Outline platelets.
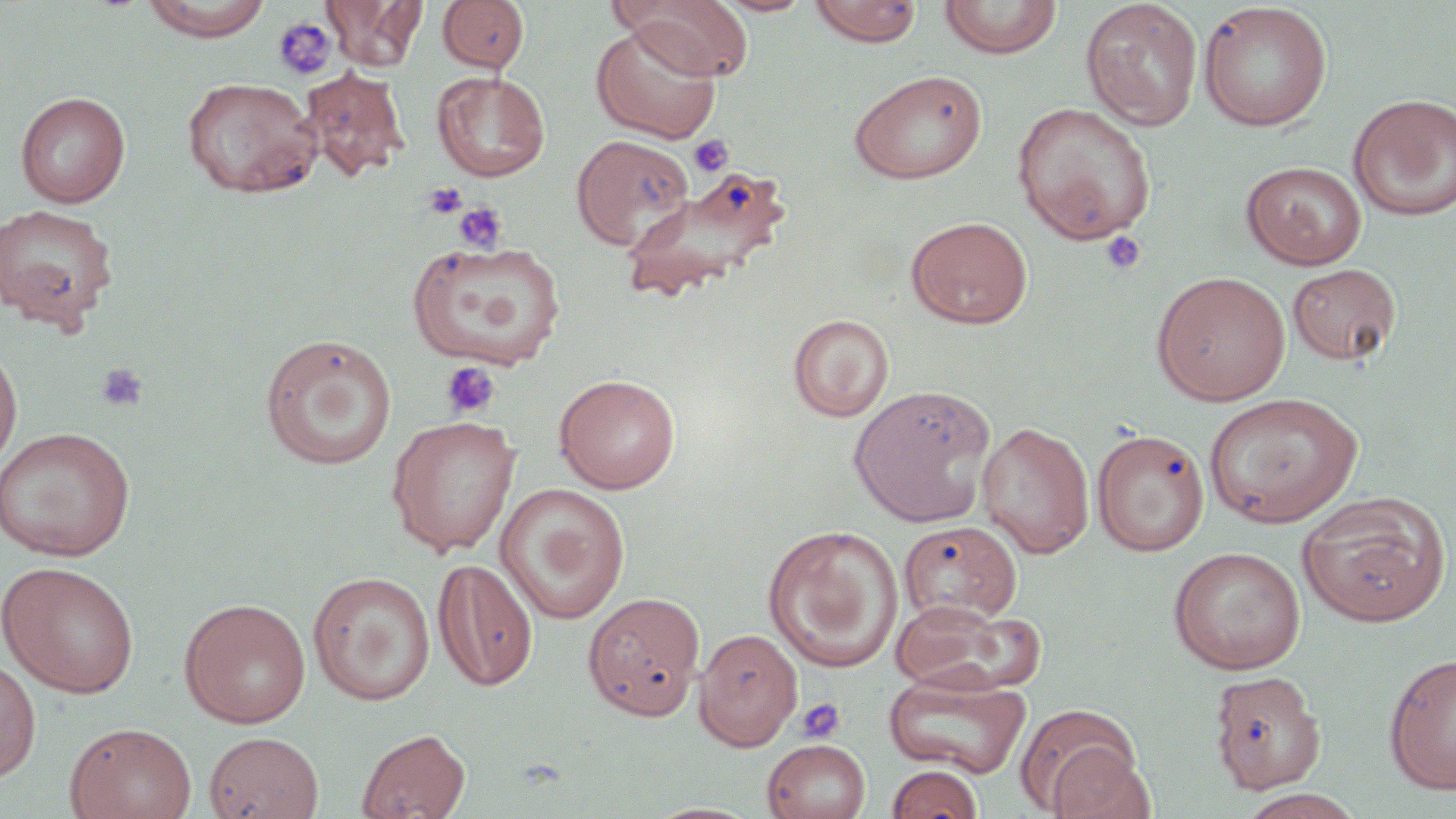
Approximate bounding boxes as named x1/y1/x2/y2 corners in pixels.
Platelets: (x1=272, y1=16, x2=338, y2=82), (x1=689, y1=134, x2=733, y2=177), (x1=423, y1=183, x2=468, y2=220), (x1=454, y1=202, x2=507, y2=253), (x1=1101, y1=230, x2=1146, y2=275), (x1=441, y1=361, x2=501, y2=419), (x1=96, y1=362, x2=148, y2=413), (x1=795, y1=697, x2=845, y2=743).

Uninfected red blood cell locations: (x1=140, y1=0, x2=275, y2=40), (x1=325, y1=0, x2=426, y2=70), (x1=438, y1=0, x2=529, y2=73), (x1=617, y1=0, x2=755, y2=80), (x1=713, y1=0, x2=814, y2=17), (x1=808, y1=0, x2=923, y2=47), (x1=939, y1=0, x2=1062, y2=59), (x1=1081, y1=1, x2=1203, y2=130), (x1=1198, y1=2, x2=1333, y2=131), (x1=591, y1=19, x2=723, y2=144), (x1=299, y1=66, x2=409, y2=182), (x1=848, y1=69, x2=988, y2=184), (x1=431, y1=70, x2=550, y2=181), (x1=182, y1=76, x2=321, y2=197), (x1=15, y1=91, x2=130, y2=207), (x1=1348, y1=93, x2=1456, y2=221), (x1=1012, y1=102, x2=1157, y2=243), (x1=572, y1=135, x2=694, y2=249), (x1=1241, y1=161, x2=1367, y2=270), (x1=617, y1=169, x2=789, y2=306), (x1=0, y1=202, x2=119, y2=329), (x1=905, y1=215, x2=1034, y2=329), (x1=406, y1=239, x2=566, y2=371), (x1=1287, y1=263, x2=1401, y2=366), (x1=1152, y1=271, x2=1291, y2=406), (x1=789, y1=314, x2=894, y2=422), (x1=259, y1=333, x2=398, y2=471), (x1=0, y1=337, x2=22, y2=476), (x1=554, y1=373, x2=681, y2=493), (x1=848, y1=386, x2=996, y2=528), (x1=1202, y1=391, x2=1364, y2=528), (x1=386, y1=414, x2=521, y2=557), (x1=977, y1=421, x2=1095, y2=558), (x1=0, y1=426, x2=136, y2=562), (x1=1092, y1=429, x2=1209, y2=556), (x1=496, y1=483, x2=631, y2=624), (x1=1297, y1=493, x2=1450, y2=627), (x1=897, y1=520, x2=1023, y2=624), (x1=763, y1=524, x2=904, y2=673), (x1=1168, y1=546, x2=1307, y2=673), (x1=432, y1=557, x2=539, y2=691), (x1=0, y1=561, x2=140, y2=698), (x1=308, y1=571, x2=435, y2=705), (x1=583, y1=591, x2=706, y2=721), (x1=179, y1=597, x2=311, y2=729), (x1=889, y1=598, x2=1039, y2=696), (x1=694, y1=628, x2=802, y2=750), (x1=1384, y1=653, x2=1456, y2=795), (x1=0, y1=658, x2=41, y2=782), (x1=883, y1=669, x2=1032, y2=778), (x1=1209, y1=670, x2=1327, y2=794), (x1=1017, y1=704, x2=1146, y2=815), (x1=64, y1=722, x2=197, y2=819), (x1=356, y1=728, x2=471, y2=818), (x1=204, y1=731, x2=324, y2=818), (x1=762, y1=738, x2=872, y2=819), (x1=886, y1=764, x2=984, y2=819), (x1=1237, y1=789, x2=1365, y2=819), (x1=644, y1=801, x2=765, y2=819). Slide-level diagnosis: negative for blood parasites. Thin blood smear. Optical microscopy. Image is 1456×819 pixels. Single field of view. 1000x magnification. May-Grünwald-Giemsa-stained preparation.